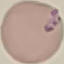 Result: malaria parasites detected. Acquired by smartphone through the microscope eyepiece. Automatically extracted cell patch, resized to 64 × 64 pixels. Thin blood smear. Giemsa stain.